Name the parasite shown.
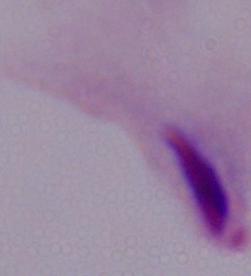
This is a trichomonad.

Photomicrograph. 1000x magnification.